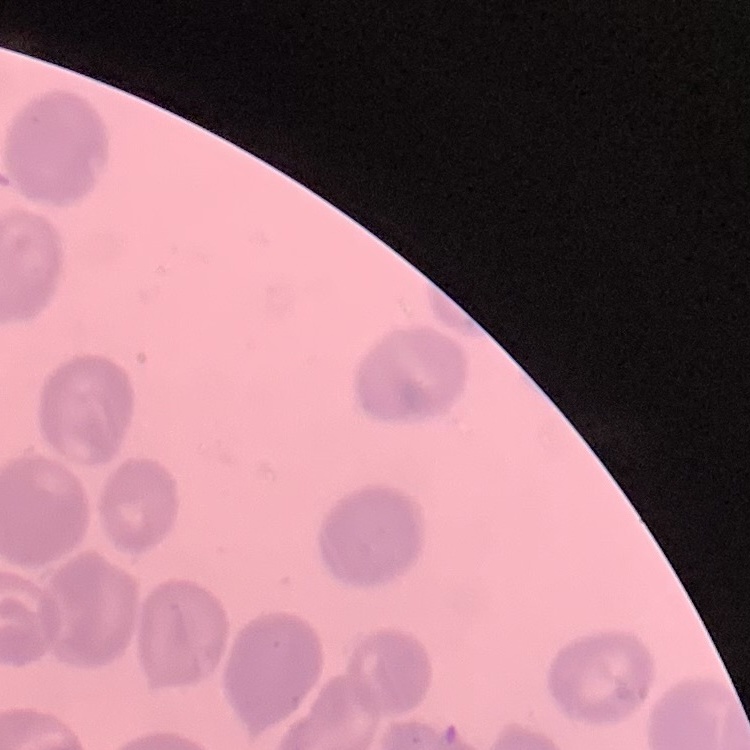
The erythrocytes exhibit no rouleaux formation. One tile cut from a larger photomicrograph. Stained with either Field's or Giemsa. Thin peripheral smear.